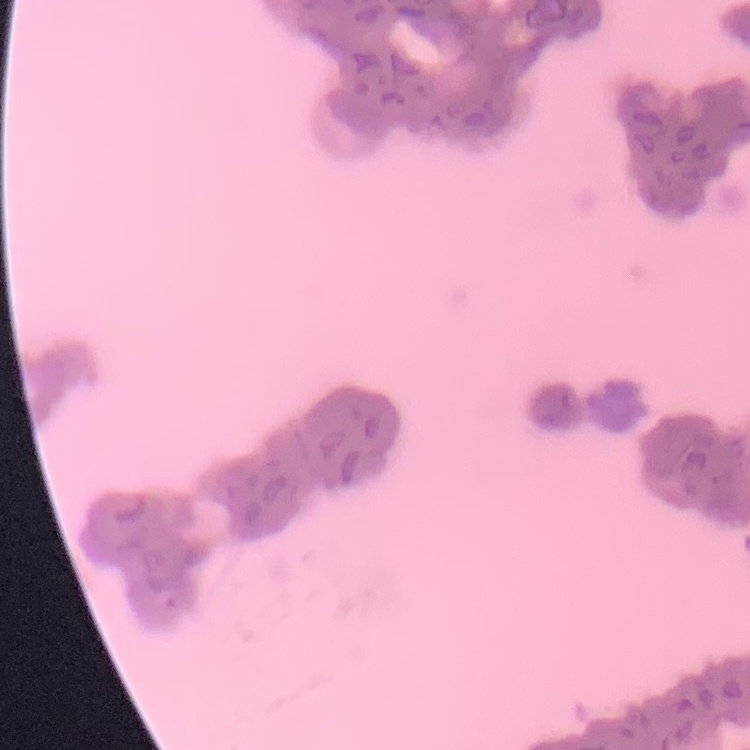
Summary:
  - Erythrocyte morphology: rouleaux formation
  - Preparation: thin peripheral smear
  - Image type: one tile cut from a larger photomicrograph
  - Stain: Field's or Giemsa